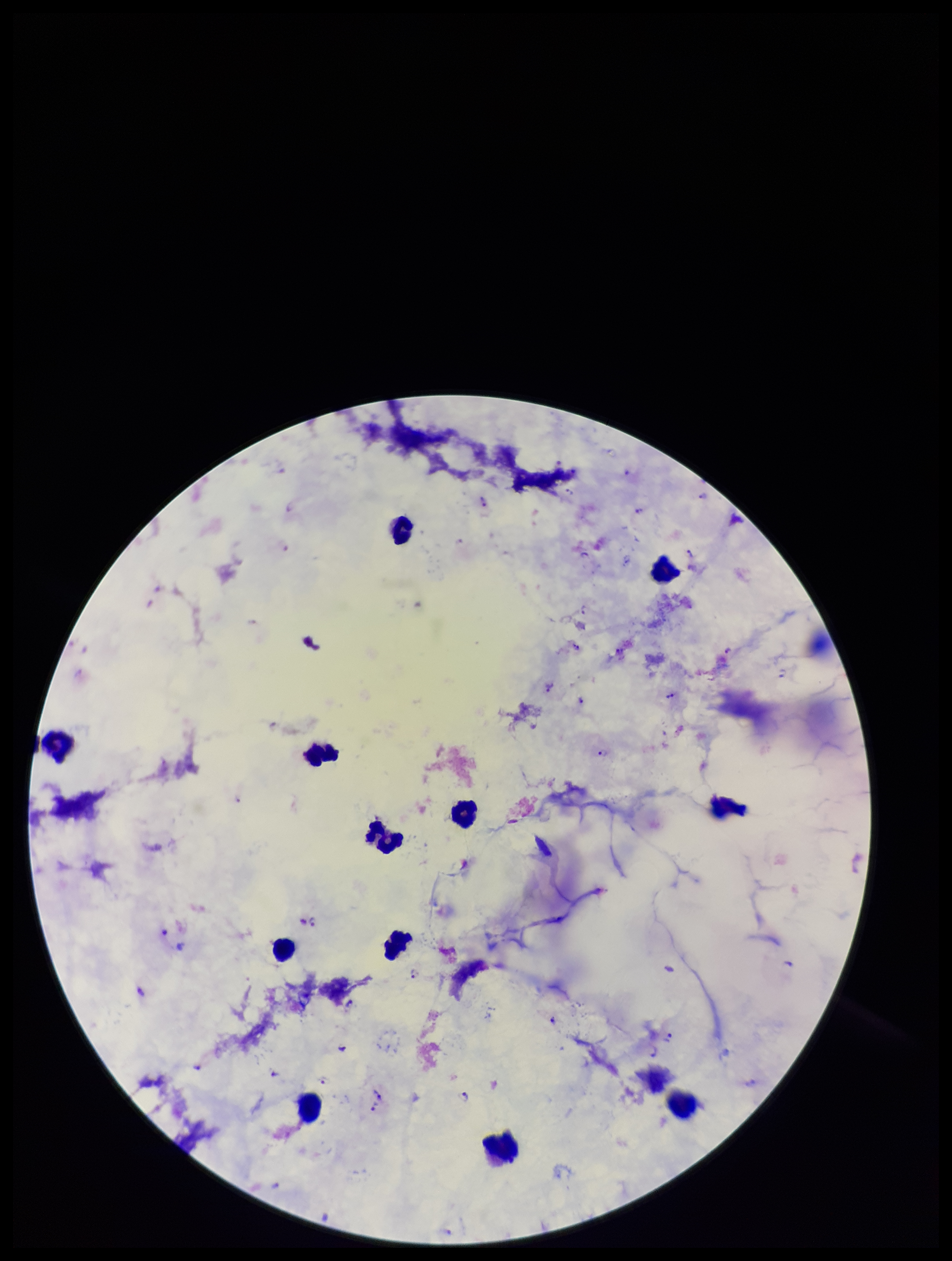
Summary:
  - Stain: Giemsa
  - Patient malaria status: infected
  - Plasmodium parasites: seen
  - Capture: smartphone photograph through the microscope eyepiece
  - Preparation: thick
  - Parasite count: 20
  - Image size: 952×1261 pixels
  - Leukocyte count: 13
  - Field of view: single
  - Species reported for this patient: Plasmodium falciparum